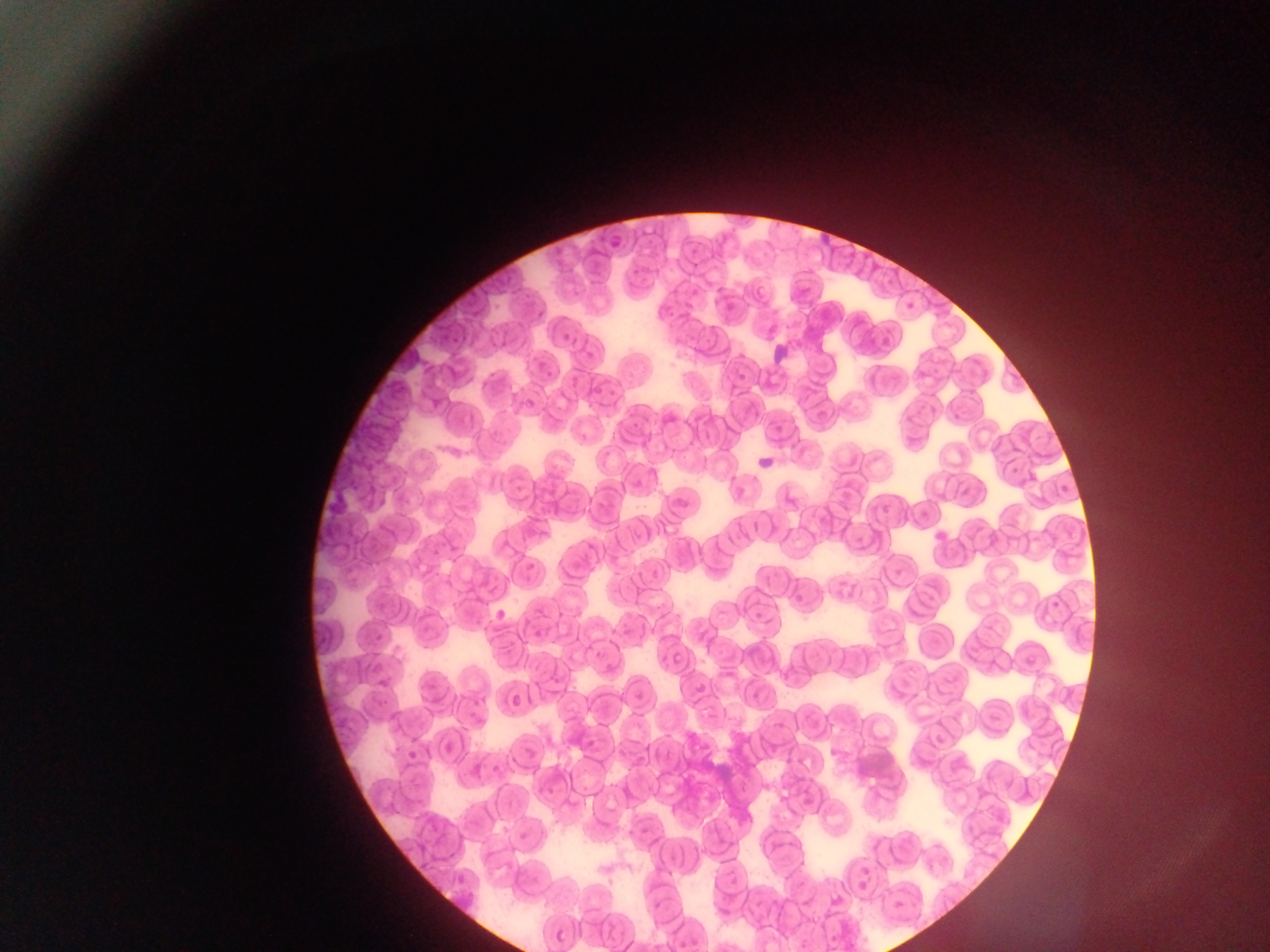

Approximate bounding boxes as (left, top, right, bottom) in pixels.
Summary:
  - Leukocyte locations: (818, 225, 835, 253), (767, 347, 798, 369), (754, 452, 779, 472), (324, 486, 353, 517)
  - Malaria parasite locations: (602, 229, 619, 256), (885, 271, 899, 290), (754, 286, 768, 297), (900, 295, 920, 317), (719, 296, 739, 313), (559, 325, 574, 345), (878, 336, 892, 348), (579, 340, 601, 361), (539, 369, 555, 382), (567, 373, 581, 393), (590, 374, 606, 402), (519, 395, 535, 408), (770, 419, 784, 436), (1006, 461, 1025, 477), (1057, 484, 1071, 496), (670, 488, 693, 514), (781, 489, 801, 509), (927, 526, 953, 545), (520, 562, 537, 583), (793, 585, 806, 602), (1047, 598, 1067, 610), (487, 603, 510, 626), (751, 603, 765, 621), (367, 621, 390, 643), (671, 648, 688, 665), (1024, 654, 1036, 665), (371, 656, 385, 676), (693, 680, 705, 694), (750, 680, 767, 704), (632, 685, 643, 704), (509, 694, 525, 708), (406, 739, 422, 760), (444, 742, 461, 753), (517, 825, 530, 845), (726, 863, 740, 889), (454, 864, 474, 887), (854, 866, 873, 877), (856, 881, 867, 891), (889, 895, 906, 918), (553, 928, 570, 946)
  - Preparation: thin blood smear
  - Country: Ghana
  - Capture: mobile-phone photograph through a microscope
  - Field of view: single
  - Image size: 1270×952 pixels